Point out each Plasmodium parasite.
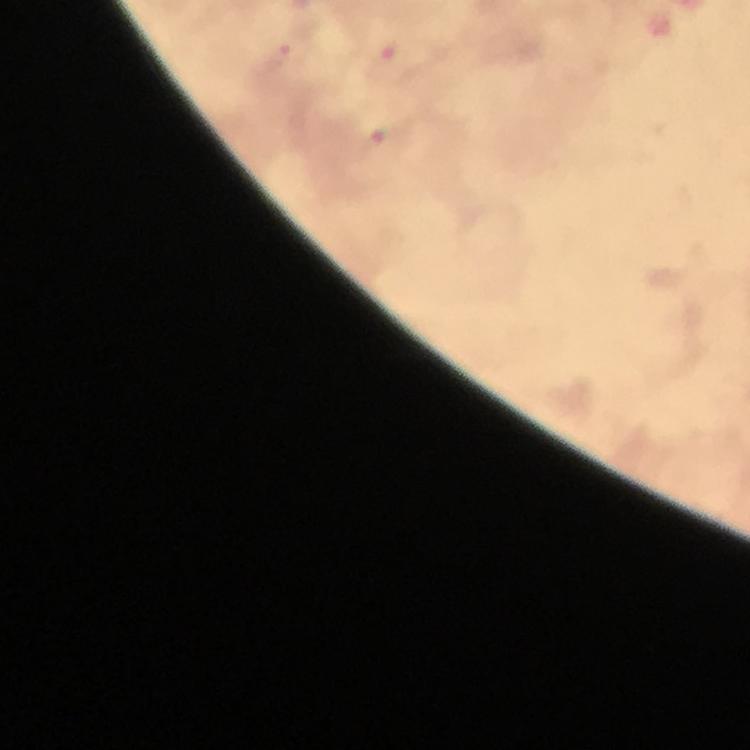
Approximate object centers, in pixels from the top-left corner.
Plasmodium parasites: (x=279, y=56).

stain: Giemsa
cropped_from: a single field of view
capture: smartphone camera through the microscope
magnification: 100x
image_size: 750×750 pixels
immersion_oil: used
preparation: thick smear
context: from a malaria diagnostic workup